Assess this cell for malaria.
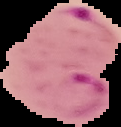

It is parasitized.

Image is 121×127 pixels. The area outside the segmented cell region is set to black. From a thin blood smear.